Locate every Plasmodium parasite by life-cycle stage, and every leukocyte.
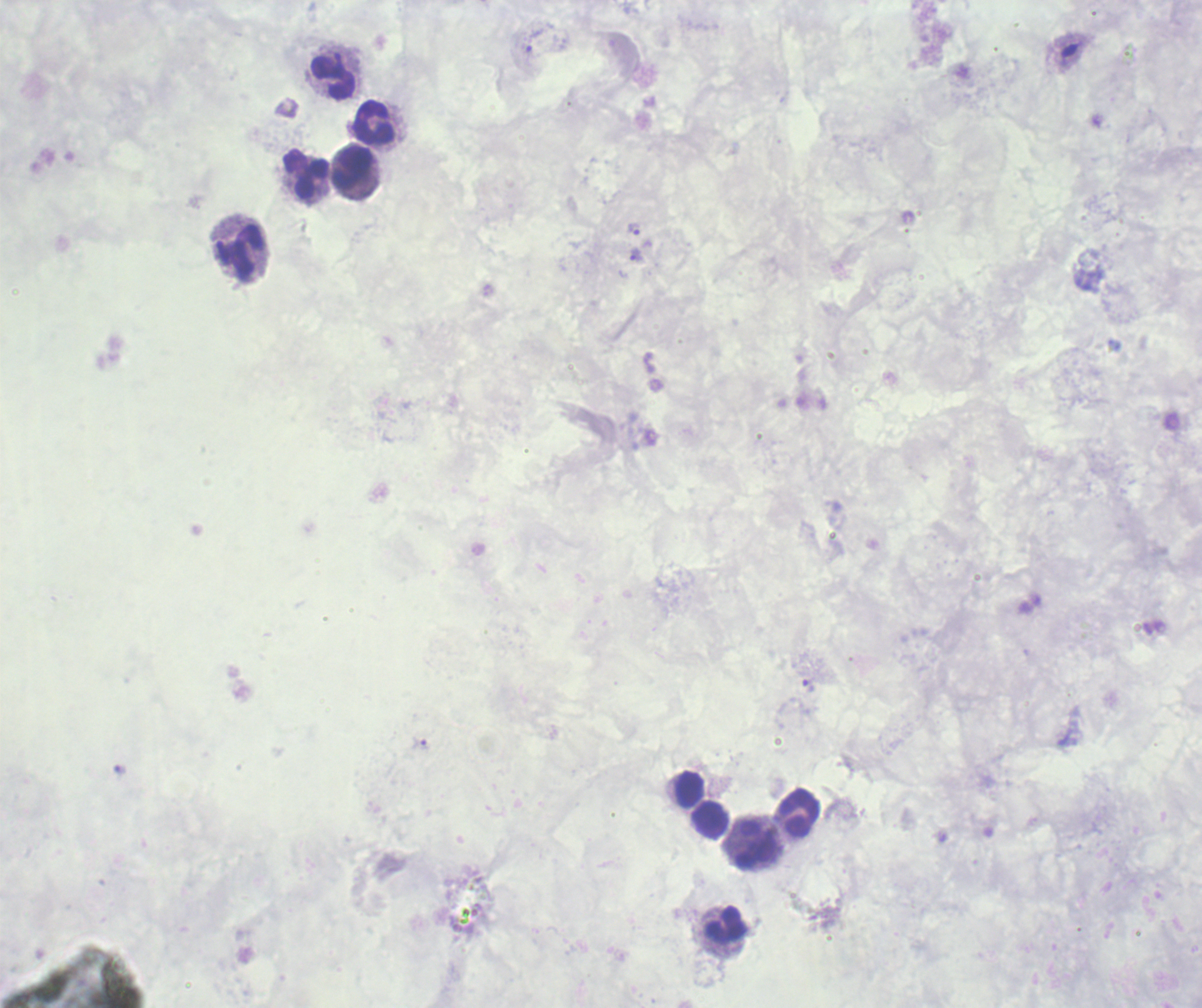
Approximate object centers, in pixels from the top-left corner.
Trophozoites: (x=534, y=40), (x=634, y=230), (x=636, y=256), (x=808, y=685), (x=422, y=743).
No schizont or gametocyte forms observed.
Leukocytes: (x=333, y=77), (x=374, y=123), (x=351, y=169), (x=305, y=173), (x=240, y=253), (x=689, y=789), (x=797, y=812), (x=709, y=819), (x=759, y=844), (x=726, y=924).

Summary:
  - Field of view: one from this slide
  - Preparation: thick blood smear
  - Magnification: 100x
  - Context: previously used in a real diagnosis
  - Image size: 1202×1008 pixels
  - Stain: Romanowsky
  - Background quality: unsatisfactory